Name the parasite shown.
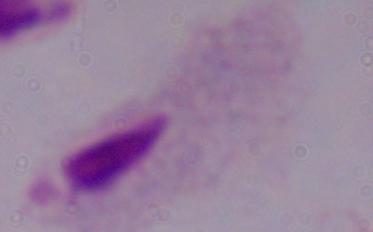

A trichomonad.

{
  "magnification": "1000x",
  "modality": "micrograph"
}